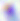
magnification = 400x
identification = Toxoplasma gondii
modality = micrograph